Locate and identify every blood parasite.
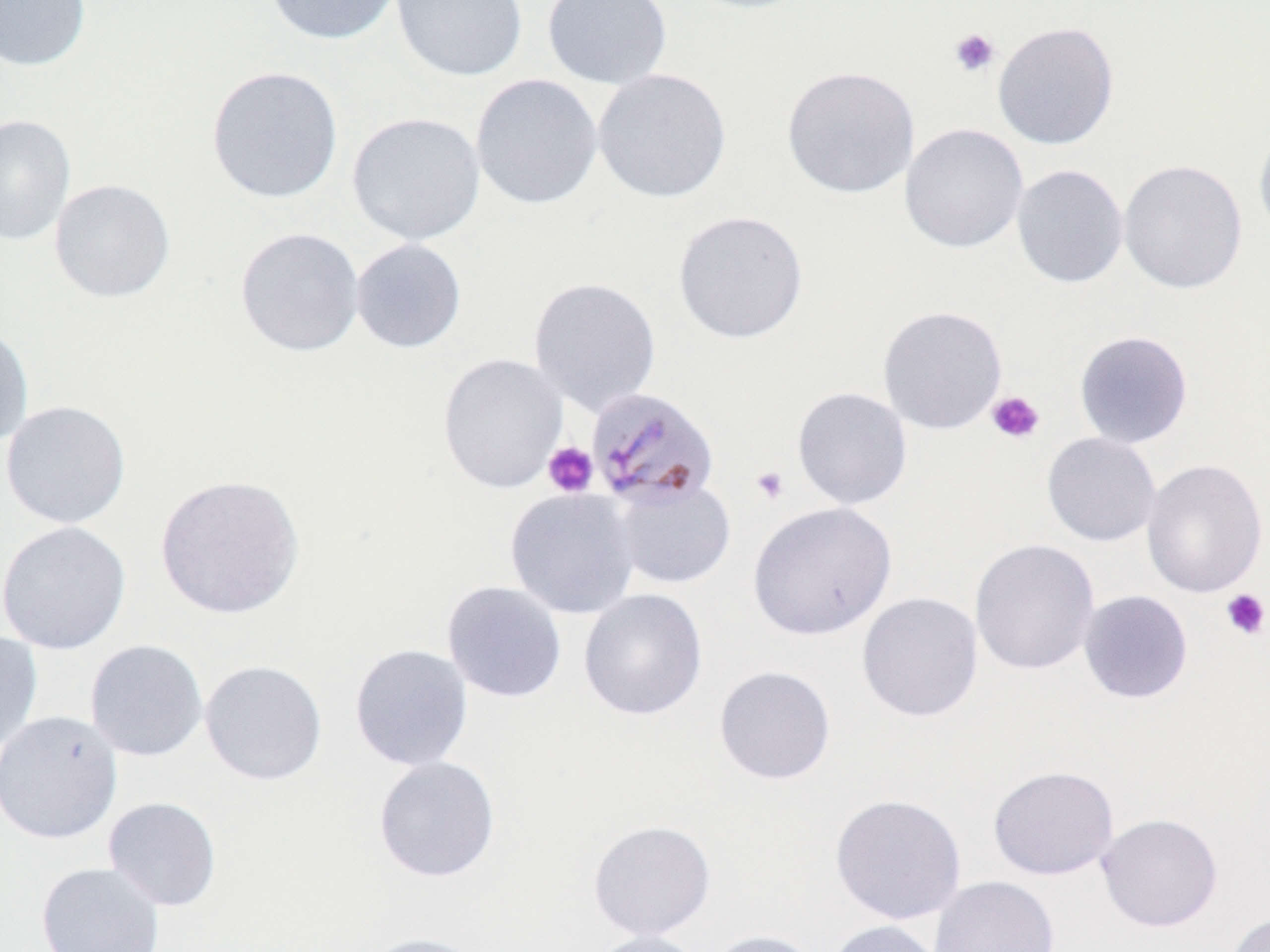

Approximate bounding boxes as (x1, y1, x2, y2) in pixels.
Plasmodium malariae-infected red blood cells: (587, 386, 720, 510).
No Plasmodium falciparum, Plasmodium ovale, Plasmodium vivax, Babesia divergens, or Trypanosoma brucei observed.

Uninfected red blood cell locations: (0, 0, 91, 72), (264, 0, 402, 45), (390, 0, 528, 82), (541, 0, 673, 89), (680, 0, 816, 15), (993, 21, 1119, 151), (206, 65, 344, 204), (781, 65, 920, 199), (592, 68, 732, 203), (470, 73, 603, 211), (347, 112, 486, 246), (0, 114, 76, 247), (1253, 120, 1270, 244), (899, 123, 1029, 254), (1118, 159, 1248, 294), (1011, 163, 1129, 289), (49, 178, 176, 303), (672, 209, 809, 345), (235, 227, 365, 357), (350, 238, 467, 354), (528, 276, 662, 416), (877, 305, 1008, 434), (0, 323, 34, 449), (1073, 330, 1193, 449), (437, 352, 569, 494), (791, 386, 913, 510), (1, 400, 132, 529), (1041, 432, 1161, 547), (1140, 458, 1268, 598), (155, 474, 305, 619), (612, 478, 736, 589), (504, 487, 640, 619), (747, 501, 897, 641), (0, 520, 133, 655), (969, 538, 1100, 675), (441, 580, 567, 703), (578, 588, 708, 721), (1078, 590, 1193, 704), (856, 591, 984, 723), (0, 630, 43, 756), (85, 639, 208, 762), (349, 643, 474, 771), (199, 659, 328, 786), (714, 665, 836, 784), (0, 710, 123, 844), (373, 755, 500, 883), (988, 765, 1119, 880), (829, 793, 967, 925), (103, 796, 222, 911), (1096, 812, 1223, 933), (588, 819, 716, 941), (36, 862, 165, 952), (929, 875, 1060, 952), (1222, 911, 1270, 952), (824, 920, 947, 952), (583, 929, 710, 952), (702, 929, 825, 952), (358, 932, 492, 952). Platelet locations: (949, 28, 1000, 77), (986, 390, 1046, 444), (543, 441, 598, 497), (749, 465, 790, 506), (1220, 589, 1270, 640). Slide-level diagnosis: Plasmodium malariae. Light microscopy. Captured at 1000x magnification. Single field of view. May-Grünwald-Giemsa stain. Thin blood smear. Image is 1270×952 pixels.